Name the cell type shown.
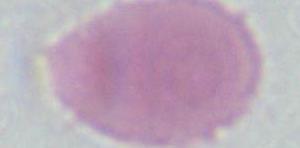

An erythrocyte.

{
  "magnification": "1000x",
  "modality": "photomicrograph"
}